Identify the parasite.
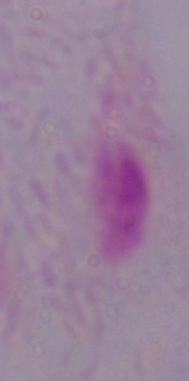

This is a trichomonad.

modality = photomicrograph
magnification = 1000x